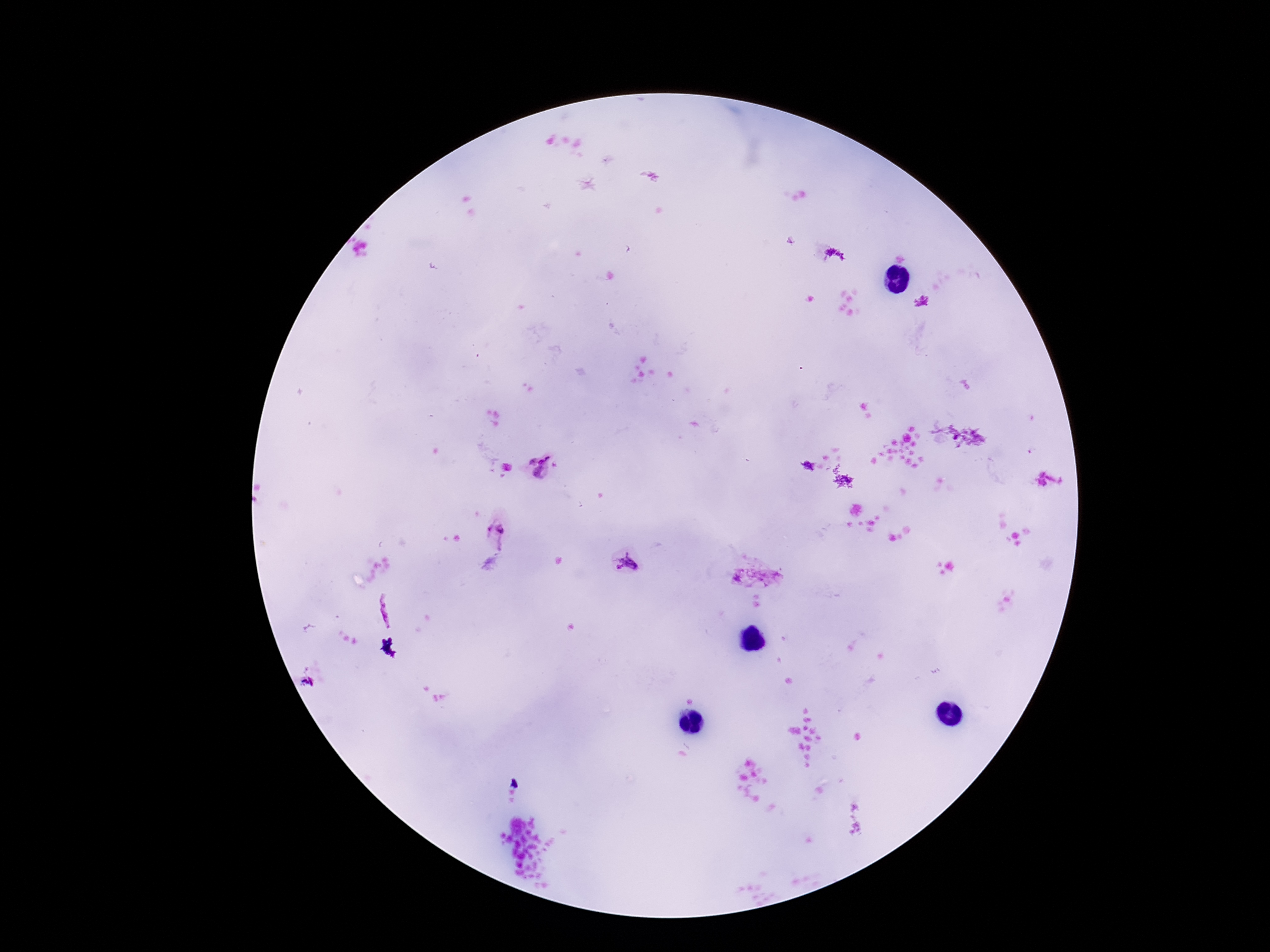 Approximate centers as (x, y) in pixels. Plasmodium parasite locations: (924, 303), (540, 467), (497, 534), (626, 563), (747, 579), (383, 613). One field from this slide. Smartphone photograph taken through the microscope eyepiece. Giemsa-stained preparation. 100x magnification. Thick peripheral-blood smear. Image is 1270×952 pixels. Patient malaria status: infected.